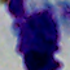 A white blood cell is seen. Micrograph. Captured at 1000x magnification.